Name the parasite shown.
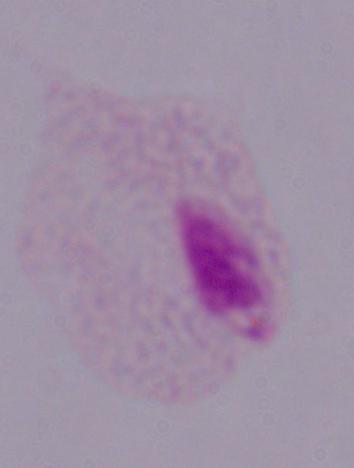

This is a trichomonad.

modality = photomicrograph
magnification = 1000x